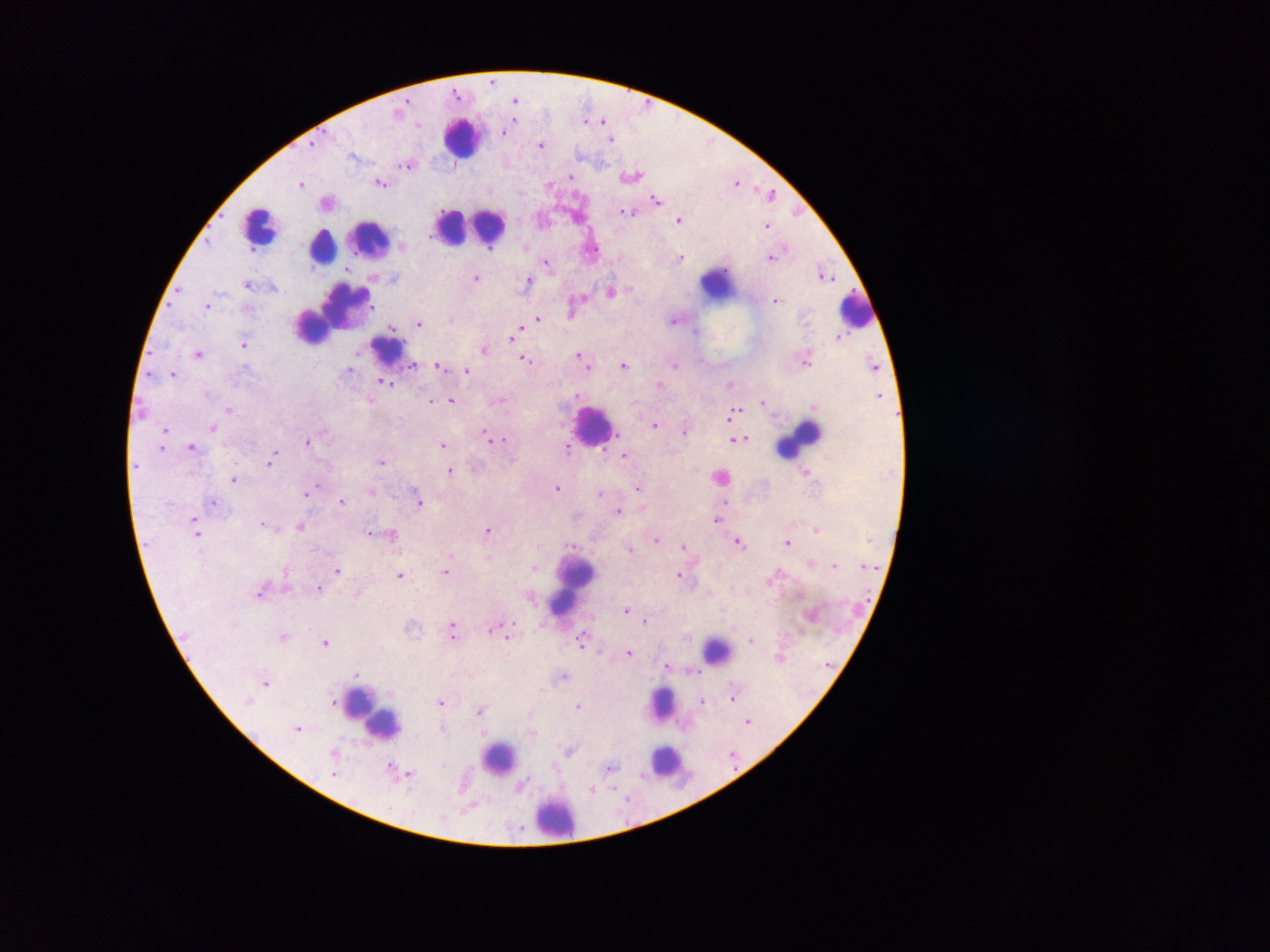

preparation = thick blood film
field of view = single
country = Ghana
image size = 1270×952 pixels
Plasmodium parasite locations = approximate centers as x y in pixels: 492 84; 457 98; 516 100; 518 121; 584 121; 602 121; 514 123; 417 126; 506 132; 612 140; 542 147; 315 148; 410 168; 569 178; 571 181; 302 184; 382 186; 656 200; 627 212; 622 213; 632 215; 680 220; 767 228; 325 231; 489 252; 773 259; 681 260; 546 265; 477 280; 530 282; 249 285; 612 294; 778 303; 375 307; 211 310; 570 318; 537 321; 674 321; 419 326; 391 330; 516 333; 510 339; 244 345; 376 346; 484 351; 578 354; 200 356; 525 360; 624 366; 437 368; 675 368; 246 369; 348 370; 589 371; 467 372; 174 377; 381 384; 732 384; 386 385; 660 386; 576 394; 207 396; 452 401; 432 403; 231 410; 738 410; 582 412; 733 414; 729 418; 655 426; 214 427; 166 431; 484 432; 686 435; 487 438; 503 440; 739 440; 308 442; 442 446; 192 447; 162 450; 567 451; 604 452; 620 455; 626 456; 272 461; 384 463; 269 466; 451 472; 807 472; 721 478; 234 481; 319 486; 640 487; 559 488; 372 493; 306 496; 598 497; 726 502; 420 503; 342 504; 213 505; 619 513; 195 519; 718 520; 261 526; 300 529; 816 531; 487 532; 200 535; 370 536; 656 543; 740 544; 788 544; 572 547; 684 548; 631 551; 695 563; 837 567; 533 568; 865 568; 338 572; 447 574; 401 576; 678 578; 773 582; 320 591; 258 596; 359 597; 626 612; 454 623; 647 623; 411 629; 490 631; 453 638; 687 638; 282 639; 508 639; 751 642; 326 644; 581 646; 601 651; 630 655; 781 660; 829 664; 670 669; 564 678; 265 685; 544 690; 734 700; 336 703; 440 704; 703 704; 250 705; 578 707; 483 710; 529 712; 749 723; 298 730; 444 730; 481 730; 532 733; 568 751; 332 754; 734 758; 612 770; 556 771; 408 774; 336 775; 527 782; 464 787; 593 790; 618 795; 630 801; 468 811; 518 830; 516 836
capture = mobile-phone photograph through a microscope
leukocyte locations = approximate centers as x y in pixels: 466 137; 254 217; 464 229; 347 251; 723 284; 851 317; 333 319; 390 352; 594 426; 808 437; 574 588; 714 650; 666 700; 376 714; 502 763; 659 765; 555 825